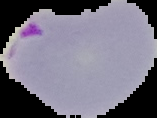
image type = cell region segmented out of the field of view; surrounding area masked to black
malaria status = parasitized
preparation = thin blood smear
image size = 157×118 pixels